Report the malaria status of this cell.
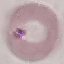

It is uninfected.

Summary:
  - Stain: Giemsa
  - Preparation: thin blood smear
  - Capture: smartphone camera at the microscope eyepiece
  - Image type: cell patch, automatically extracted from a larger field of view and resized to 64 × 64 pixels